Name the parasite shown.
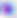

Toxoplasma gondii.

Micrograph. Captured at 400x magnification.